Assess the morphology of the erythrocytes.
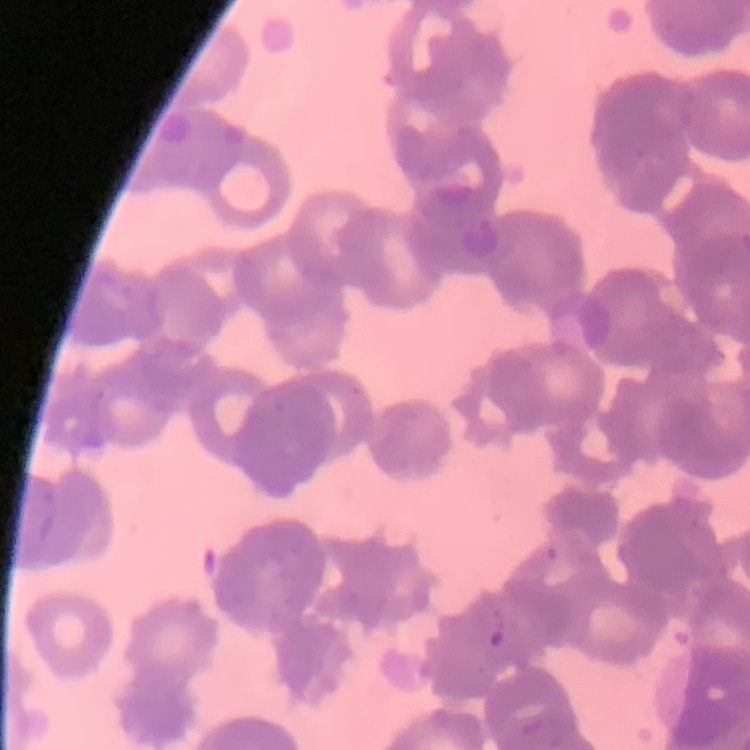

Rouleaux formation.

Thin peripheral smear. One tile cut from a larger photomicrograph. Field's or Giemsa stain.